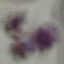 Result: no malaria parasites seen. Giemsa stain. Acquired by smartphone through the microscope eyepiece. Thin smear of blood. Automatically extracted cell patch, resized to 64 × 64 pixels.